Classify this cell by malaria status.
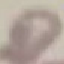

Uninfected.

{
  "capture": "smartphone camera at the microscope eyepiece",
  "preparation": "thin smear",
  "image_type": "automatically extracted cell patch, resized to 64 × 64 pixels",
  "stain": "Giemsa"
}